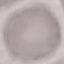
result: no malaria parasites detected
image_type: automatically extracted cell patch, resized to 64 × 64 pixels
preparation: thin blood film
stain: Giemsa
capture: smartphone through the microscope eyepiece